Outline each Plasmodium falciparum-infected red blood cell.
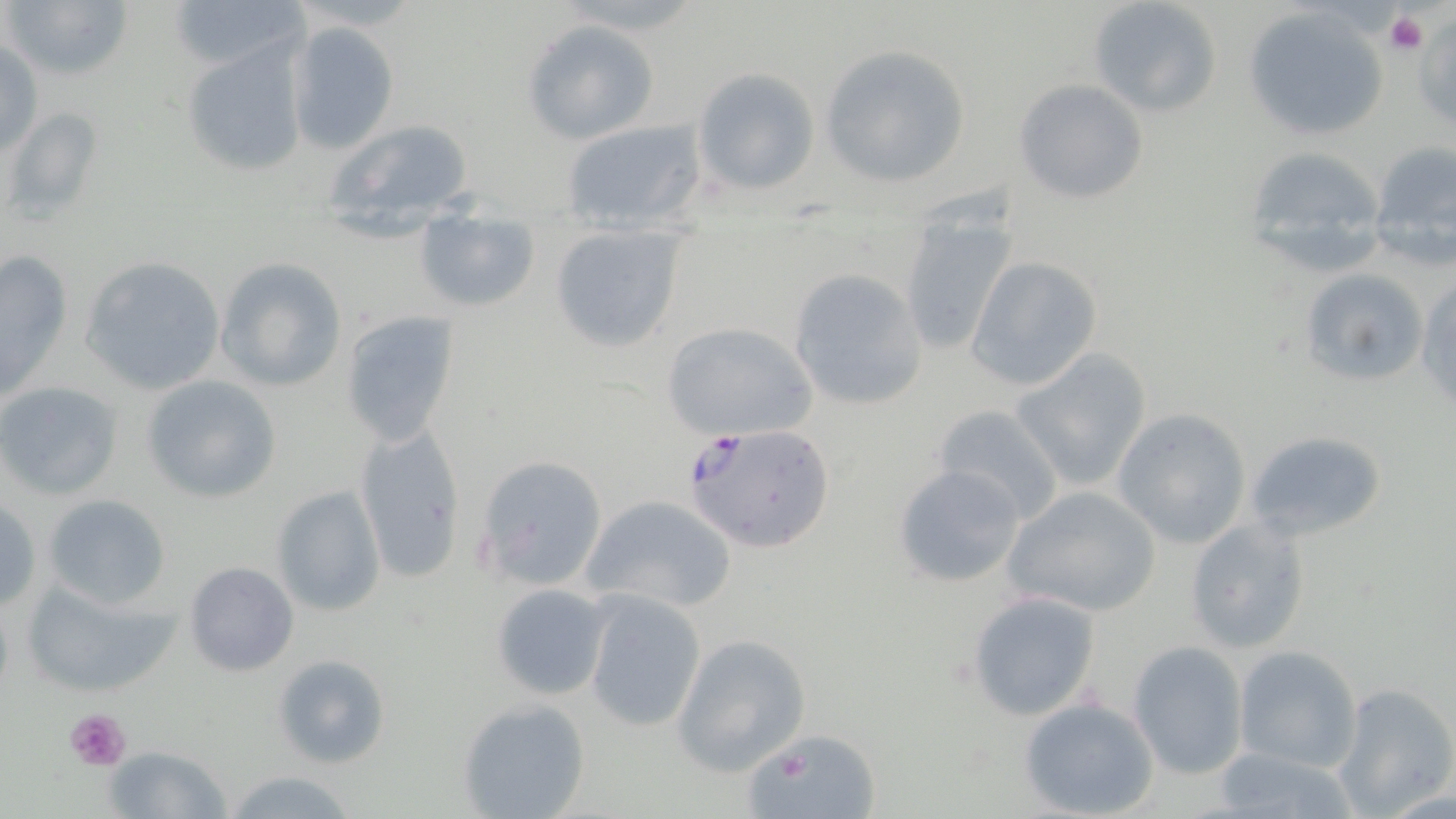
Approximate bounding boxes as (x1, y1, x2, y2) in pixels.
Plasmodium falciparum-infected red blood cells: (685, 422, 837, 554).

Summary:
  - Platelet locations: (1389, 9, 1445, 79), (1386, 11, 1426, 56), (63, 707, 134, 774)
  - Uninfected red blood cell locations: (4, 0, 134, 84), (168, 0, 304, 79), (1086, 0, 1221, 117), (1242, 7, 1389, 141), (521, 19, 660, 145), (288, 21, 400, 153), (1, 36, 42, 159), (177, 38, 308, 179), (821, 46, 971, 187), (692, 66, 819, 196), (1014, 79, 1148, 204), (4, 106, 103, 225), (319, 117, 478, 241), (560, 119, 707, 234), (1366, 141, 1455, 265), (1241, 143, 1393, 273), (894, 203, 1020, 360), (414, 205, 541, 312), (547, 223, 689, 355), (1, 247, 73, 397), (78, 256, 228, 395), (214, 257, 345, 393), (967, 257, 1101, 392), (1302, 267, 1427, 385), (788, 269, 929, 412), (1417, 273, 1456, 418), (338, 312, 458, 447), (663, 321, 817, 440), (1013, 350, 1150, 490), (141, 375, 281, 504), (1, 382, 123, 500), (932, 403, 1064, 524), (1111, 408, 1252, 549), (354, 424, 467, 582), (1243, 427, 1391, 546), (472, 452, 610, 591), (894, 463, 1028, 589), (1002, 483, 1163, 618), (271, 486, 387, 617), (42, 491, 175, 612), (579, 493, 737, 614), (0, 497, 43, 614), (1185, 516, 1311, 655), (184, 561, 299, 677), (19, 575, 182, 699), (488, 583, 612, 701), (583, 590, 708, 732), (967, 590, 1103, 721), (671, 633, 812, 775), (1127, 639, 1249, 779), (1233, 645, 1362, 772), (271, 653, 390, 771), (1334, 684, 1456, 815), (456, 696, 591, 819), (1018, 697, 1159, 819), (749, 725, 877, 818), (103, 745, 232, 818), (1212, 746, 1357, 819), (221, 768, 360, 819)
  - Slide-level diagnosis: Plasmodium falciparum
  - Image size: 1456×819 pixels
  - Modality: optical microscopy
  - Field of view: one of a larger specimen
  - Magnification: 1000x
  - Stain: May-Grünwald-Giemsa
  - Preparation: thin blood film